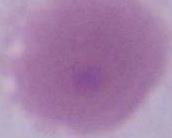
Summary:
  - Magnification: 1000x
  - Modality: micrograph
  - Identification: erythrocyte